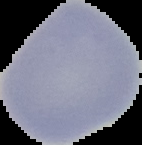
image_size: 142×145 pixels
image_type: cell region segmented out of the field of view; surrounding area masked to black
malaria_status: uninfected
preparation: thin blood smear